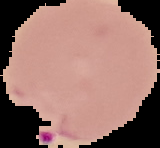

Cell region segmented out of the field of view; the surrounding area is masked to black. Result: Plasmodium parasites identified. From a thin blood smear. Image is 160×148 pixels.